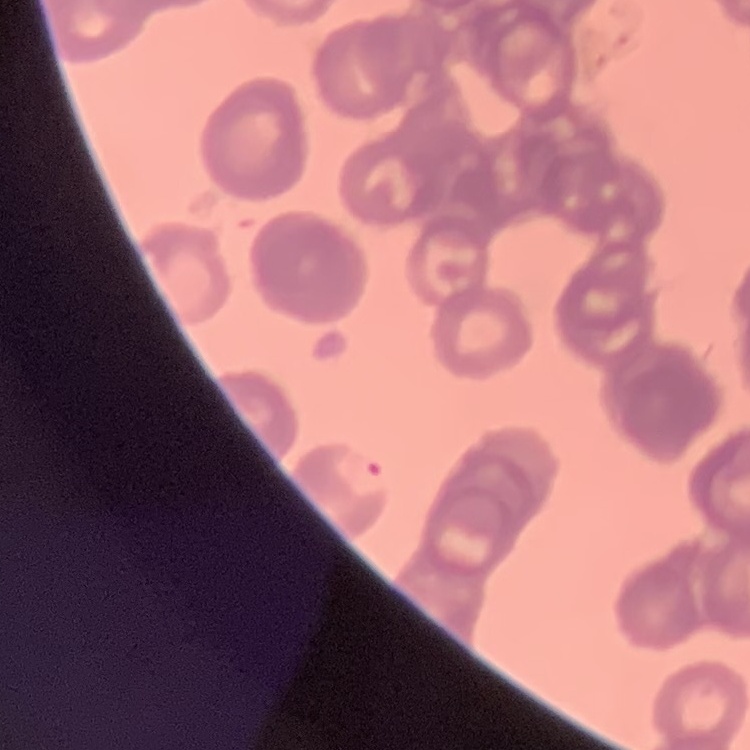
Summary:
  - Red blood cell morphology: rouleaux formation
  - Stain: Field's or Giemsa
  - Image type: one tile cut from a larger photomicrograph
  - Preparation: thin peripheral smear